Classify this cell by malaria status.
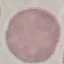

Uninfected.

Giemsa stain. Cell patch, automatically extracted from a larger field of view and resized to 64 × 64 pixels. Acquired by smartphone through the microscope eyepiece. Thin smear of blood.